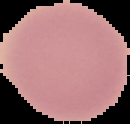 From a thin blood film. Malaria status: uninfected. Image is 130×124 pixels. Cell region segmented out of the field of view; the surrounding area is masked to black.